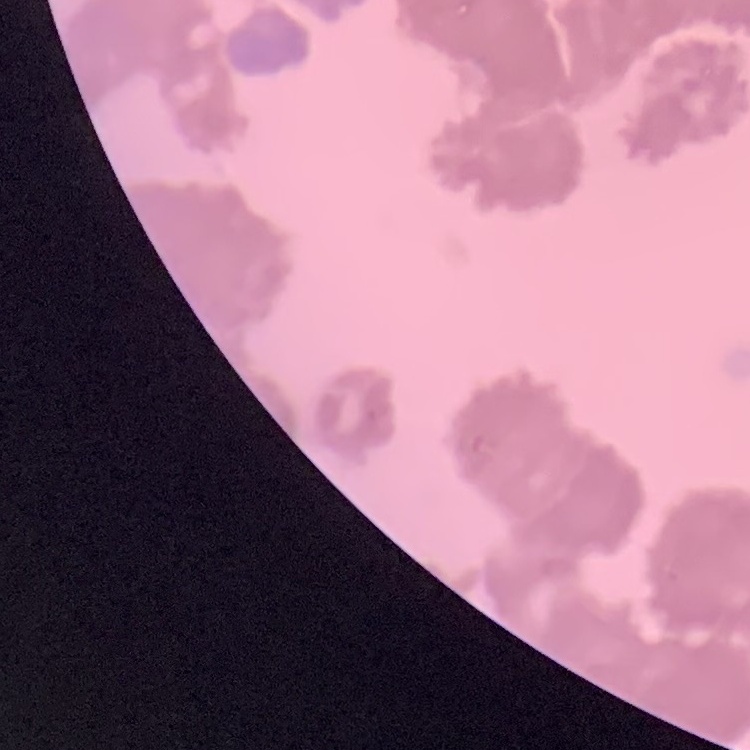

Summary:
  - Red blood cell morphology: rouleaux formation
  - Stain: Field's or Giemsa
  - Preparation: thin blood film
  - Image type: square crop of a larger photomicrograph